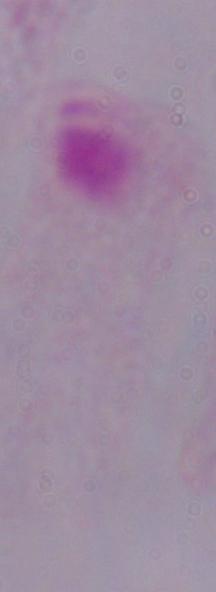
Summary:
  - Identification: trichomonad
  - Modality: photomicrograph
  - Magnification: 1000x